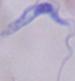
{
  "identification": "trypanosome",
  "modality": "photomicrograph",
  "magnification": "1000x"
}